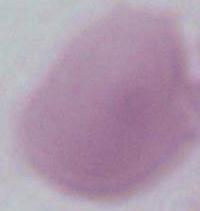
Summary:
  - Magnification: 1000x
  - Identification: erythrocyte
  - Modality: micrograph